Report the malaria status of this cell.
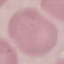

Uninfected.

Summary:
  - Stain: Giemsa
  - Capture: smartphone camera at the microscope eyepiece
  - Preparation: thin smear
  - Image type: cell patch, automatically extracted from a larger field of view and resized to 64 × 64 pixels